Assess for malaria.
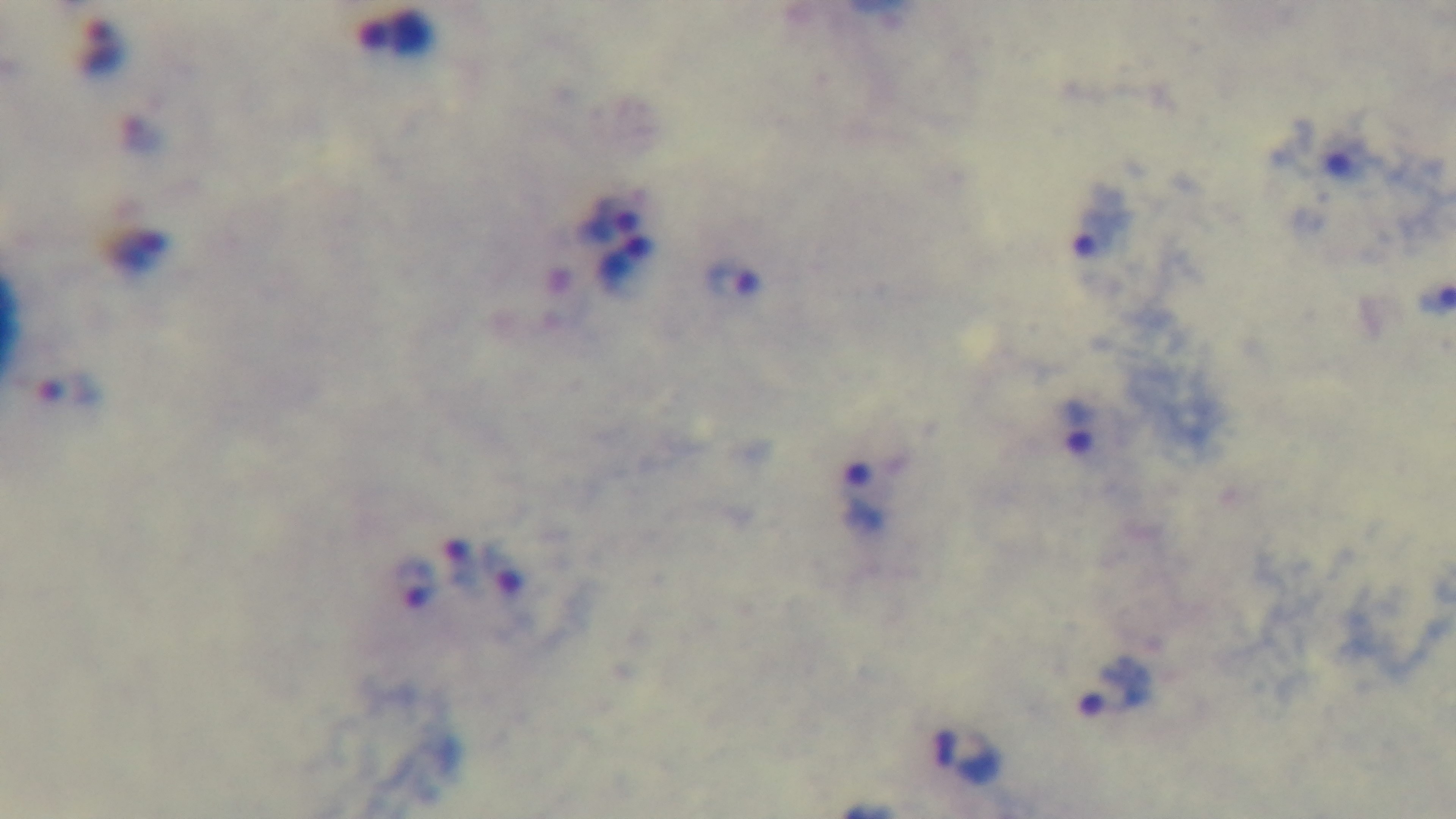
Infected.

One field from the slide. Giemsa stain. Mounted 4K digital camera. 100x oil-immersion objective. Preparation: thick smear. Light microscopy.